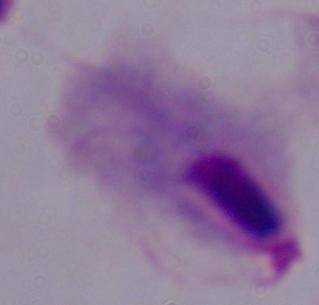

Summary:
  - Identification: trichomonad
  - Magnification: 1000x
  - Modality: photomicrograph